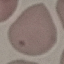 Malaria status: uninfected. Thin blood film. Giemsa-stained preparation. Automatically extracted cell patch, resized to 64 × 64 pixels. Acquired by smartphone through the microscope eyepiece.